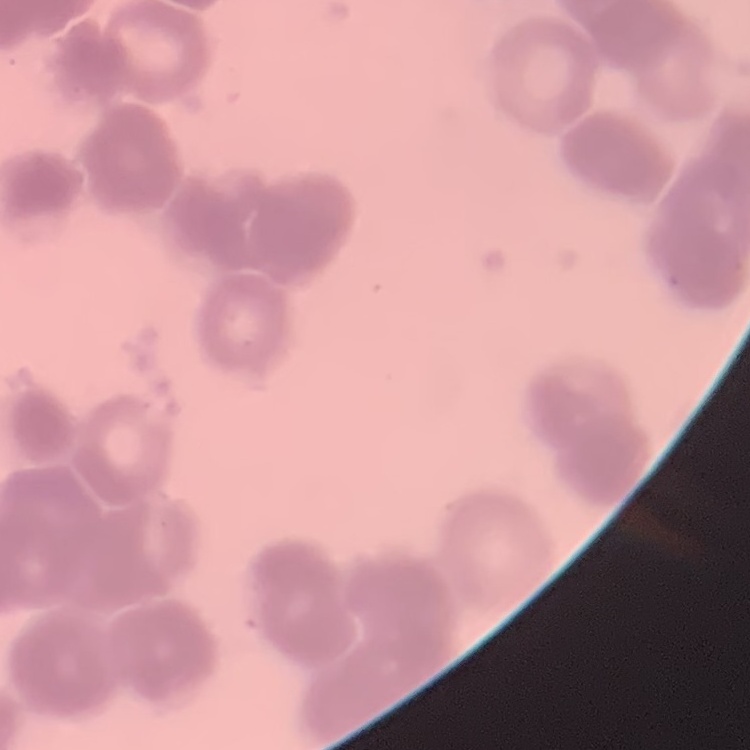
red_blood_cell_morphology: rouleaux formation
preparation: thin blood smear
stain: Field's or Giemsa
image_type: square crop of a larger photomicrograph